Find the cells and give the type of each one.
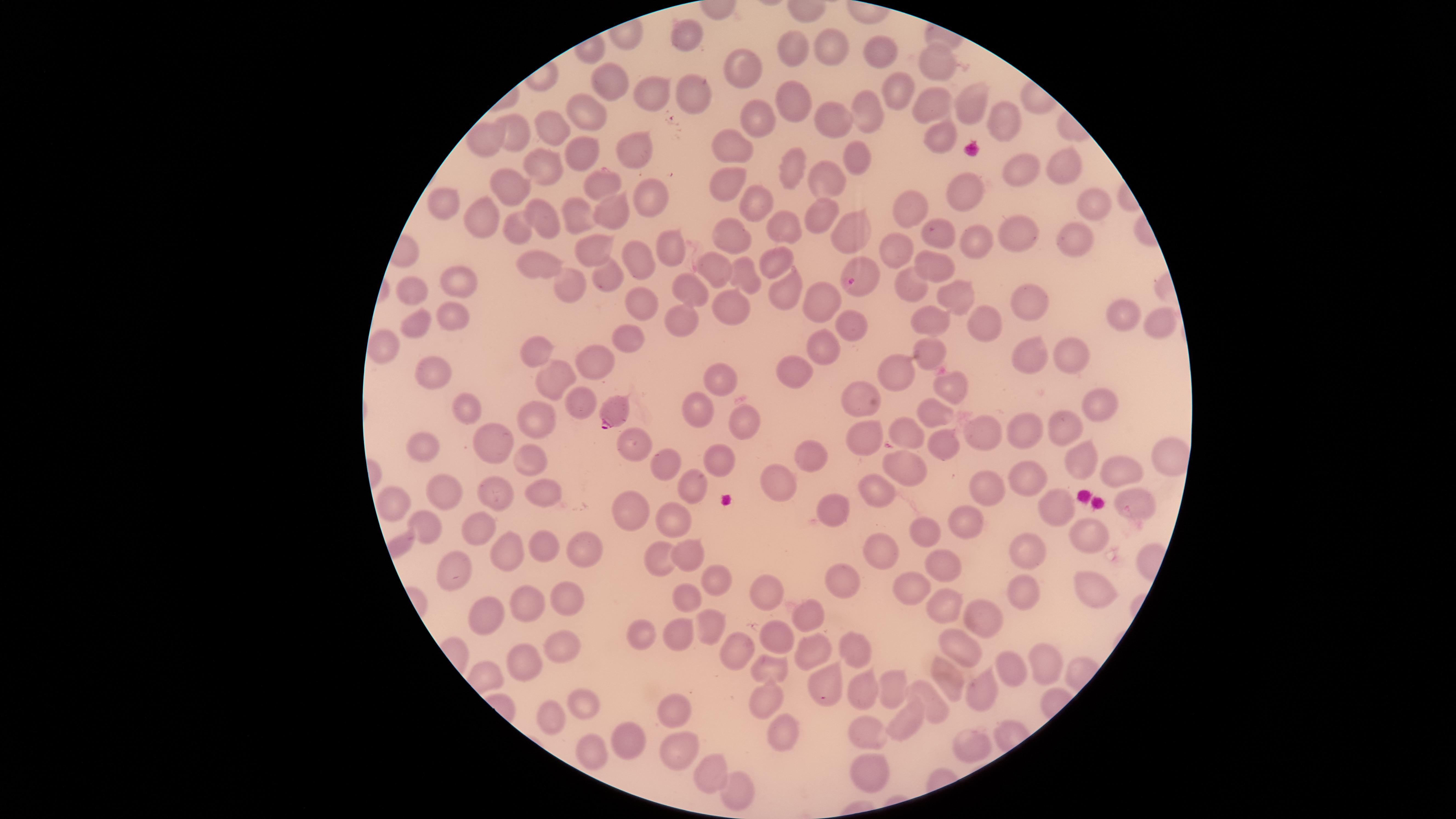

Approximate marker points as (x, y) in pixels.
Parasitized red blood cells: (598, 181), (862, 279), (612, 415).
Uninfected red blood cells: (684, 37), (830, 45), (789, 47), (879, 50), (938, 62), (745, 71), (611, 86), (894, 90), (655, 95), (694, 95), (785, 98), (969, 98), (937, 102), (585, 113), (867, 117), (998, 117), (759, 120), (834, 123), (553, 130), (515, 134), (942, 135), (480, 140), (634, 146), (738, 146), (578, 152), (852, 159), (1063, 163), (537, 166), (787, 172), (1026, 175), (724, 184), (824, 184), (977, 188), (514, 190), (646, 195), (450, 202), (758, 204), (909, 207), (1088, 207), (818, 215), (484, 218), (609, 218), (572, 220), (543, 222), (787, 231), (843, 231), (937, 233), (1017, 233), (516, 235), (737, 239), (1077, 239), (969, 242), (667, 249), (594, 252), (891, 252), (774, 260), (633, 261), (716, 266), (930, 266), (543, 269), (608, 280), (740, 280), (463, 284), (571, 285), (909, 287), (782, 291), (414, 293), (959, 295), (688, 298), (821, 300), (645, 302), (1034, 304), (731, 305), (1116, 315), (452, 318), (930, 320), (847, 324), (682, 325), (987, 327), (1161, 328), (409, 330), (627, 337), (382, 348), (928, 348), (826, 350), (1077, 355), (592, 358), (1040, 358), (536, 359), (428, 367), (899, 372), (796, 373), (548, 380), (723, 383), (951, 387), (859, 400), (1099, 402), (465, 403), (579, 403), (694, 409), (934, 415), (533, 419), (747, 420), (909, 430), (1067, 430), (977, 431), (1025, 431), (501, 437), (860, 438), (420, 439), (633, 444), (943, 446), (530, 452), (809, 452), (715, 457), (1165, 461), (667, 466), (1076, 467), (898, 468), (1027, 476), (1120, 478), (694, 479), (775, 483), (982, 484), (441, 486), (877, 488), (493, 489), (540, 489), (390, 499), (1133, 503), (632, 506), (1063, 506), (828, 509), (675, 519), (426, 530), (961, 530), (476, 532), (1086, 534), (924, 535), (541, 541), (509, 546), (585, 549), (687, 550), (1035, 551), (881, 554), (947, 555), (658, 558), (448, 577), (846, 578), (713, 581), (1094, 587), (915, 588), (1020, 589), (767, 593), (569, 598), (527, 600), (938, 600), (685, 603), (801, 614), (479, 616), (980, 619), (708, 627), (637, 629), (681, 637), (775, 640), (558, 642), (734, 647), (851, 647), (961, 648), (815, 652), (522, 660), (1045, 661), (1001, 668), (771, 671), (893, 682), (949, 683), (860, 692), (824, 694), (766, 696), (978, 696), (920, 699), (580, 702), (674, 710), (547, 720), (910, 724), (777, 729), (620, 734), (869, 735), (976, 743), (675, 748), (589, 749), (705, 769), (865, 773), (730, 793).
No white blood cells identified.

Thin blood film. Species: Plasmodium falciparum. One field of view of the specimen. Image is 1456×819 pixels. Smartphone photograph through the microscope eyepiece. The visible region is circular. Giemsa stain.